Assess this cell for malaria.
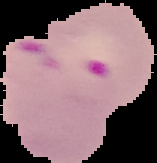
Parasitized.

Summary:
  - Preparation: thin blood smear
  - Image size: 157×163 pixels
  - Image type: segmented cell region on a black background